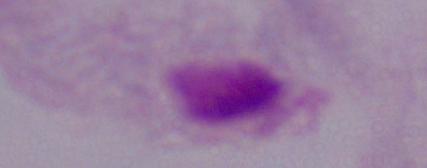

{
  "magnification": "1000x",
  "modality": "micrograph",
  "identification": "trichomonad"
}